Assess this cell for malaria.
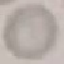
It is uninfected.

Automatically extracted cell patch, resized to 64 × 64 pixels. Acquired by smartphone through the microscope eyepiece. Giemsa stain. Thin smear of blood.